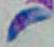

1000x magnification. Micrograph. Toxoplasma gondii is seen.